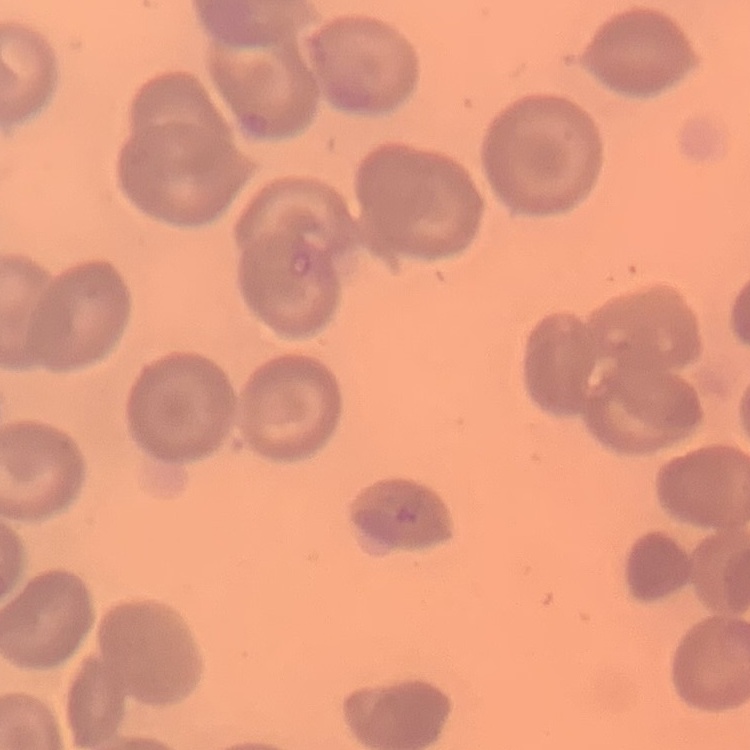

Summary:
  - Erythrocyte morphology: no rouleaux formation
  - Image type: square crop of a larger photomicrograph
  - Preparation: thin peripheral smear
  - Stain: Field's or Giemsa